Give the extent of all Plasmodium falciparum-infected red blood cells.
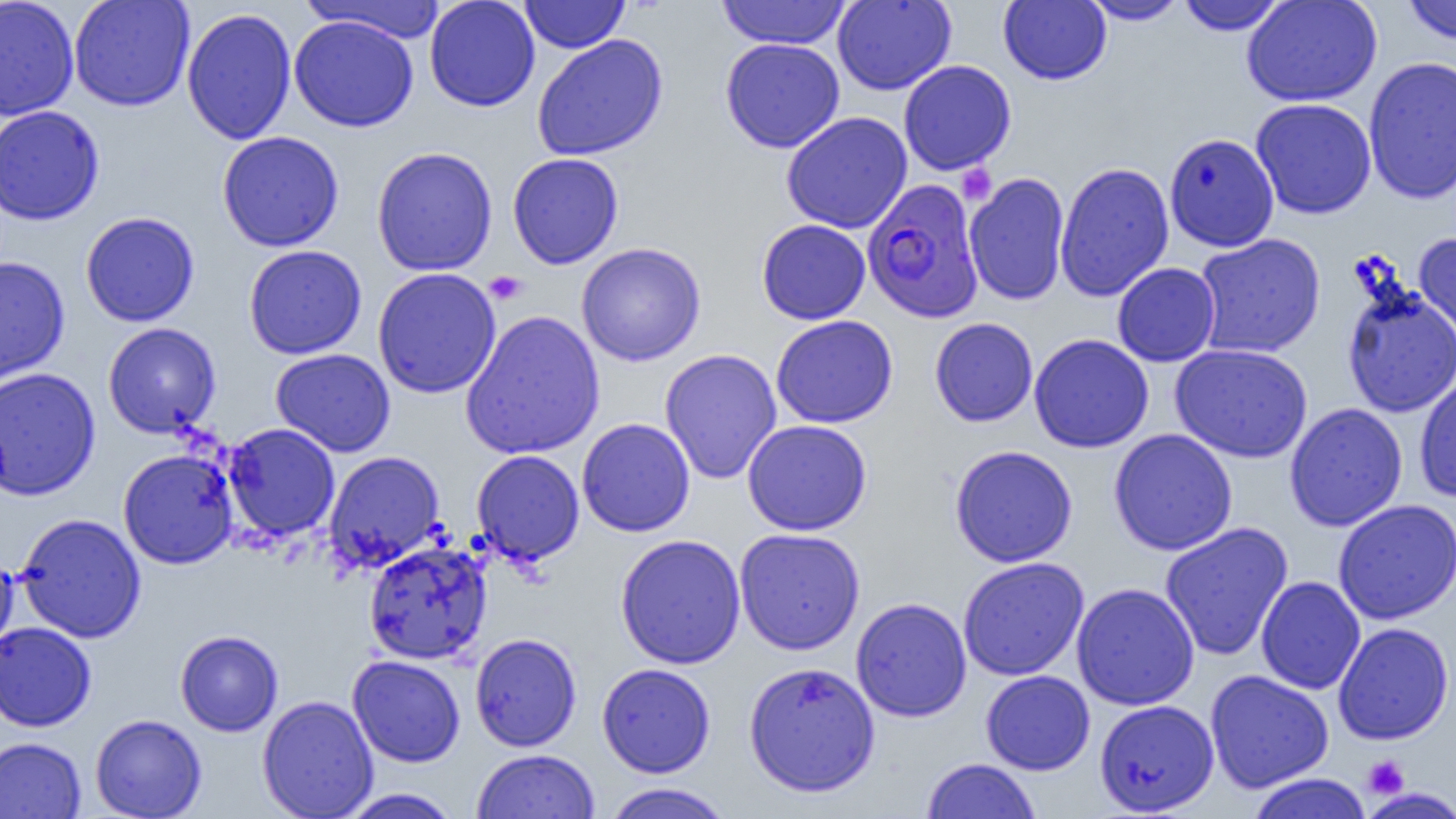

Approximate bounding boxes as (x1, y1, x2, y2) in pixels.
Plasmodium falciparum-infected red blood cells: (862, 179, 984, 323).

{
  "slide_level_diagnosis": "Plasmodium falciparum",
  "magnification": "1000x",
  "preparation": "thin blood film",
  "modality": "optical microscopy",
  "platelet_locations": "approximate bounding boxes as (x1, y1, x2, y2) in pixels: (955, 163, 997, 205), (484, 270, 528, 305), (1363, 756, 1409, 798)",
  "image_size": "1456×819 pixels",
  "field_of_view": "one of a larger specimen",
  "uninfected_red_blood_cell_locations": "approximate bounding boxes as (x1, y1, x2, y2) in pixels: (0, 0, 79, 120), (68, 0, 195, 112), (424, 0, 540, 112), (520, 0, 630, 54), (998, 0, 1111, 85), (1080, 0, 1191, 25), (1176, 0, 1289, 35), (1242, 0, 1382, 107), (1401, 0, 1456, 45), (302, 1, 448, 43), (715, 1, 852, 49), (832, 1, 956, 95), (181, 8, 297, 145), (289, 14, 419, 132), (531, 34, 668, 160), (720, 38, 845, 154), (1363, 56, 1456, 204), (898, 60, 1016, 175), (1250, 98, 1377, 219), (0, 105, 105, 226), (781, 111, 912, 233), (217, 131, 344, 252), (1164, 132, 1279, 252), (371, 147, 498, 276), (507, 152, 624, 269), (1054, 161, 1174, 301), (964, 172, 1070, 306), (80, 211, 200, 327), (756, 219, 871, 324), (1414, 231, 1456, 348), (1194, 233, 1326, 359), (576, 242, 706, 366), (243, 244, 367, 360), (0, 256, 70, 387), (1112, 262, 1221, 367), (372, 267, 502, 399), (1340, 283, 1456, 418), (460, 310, 605, 461), (771, 315, 898, 428), (929, 317, 1038, 426), (103, 322, 221, 438), (114, 324, 226, 568), (1029, 333, 1154, 453), (1170, 343, 1313, 463), (270, 348, 396, 457), (659, 348, 782, 484), (0, 366, 100, 501), (1414, 374, 1456, 503), (1284, 402, 1408, 531), (577, 417, 695, 536), (742, 419, 872, 536), (223, 423, 340, 542), (1108, 429, 1238, 556), (949, 445, 1078, 567), (118, 448, 239, 569), (471, 449, 585, 565), (323, 451, 445, 571), (1332, 498, 1456, 625), (15, 513, 146, 643), (1159, 521, 1293, 662), (735, 527, 865, 655), (615, 533, 747, 670), (363, 541, 492, 665), (0, 550, 18, 657), (957, 557, 1089, 681), (1255, 575, 1366, 695), (1071, 582, 1199, 711), (850, 597, 972, 722), (0, 622, 97, 732), (1333, 622, 1453, 745), (175, 630, 284, 737), (470, 633, 582, 751), (347, 655, 465, 767), (742, 661, 881, 798), (597, 662, 716, 778), (980, 670, 1095, 775), (1205, 670, 1334, 793), (257, 695, 378, 819), (1094, 699, 1219, 816), (90, 714, 207, 818), (0, 736, 86, 819), (471, 749, 600, 819), (922, 758, 1041, 819), (1246, 773, 1373, 819), (600, 782, 735, 819), (1359, 787, 1456, 818), (337, 788, 463, 818)"
}